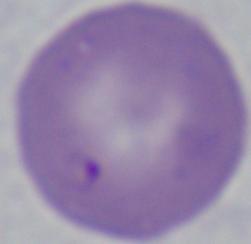 A Babesia parasite is seen. Micrograph. Captured at 1000x magnification.